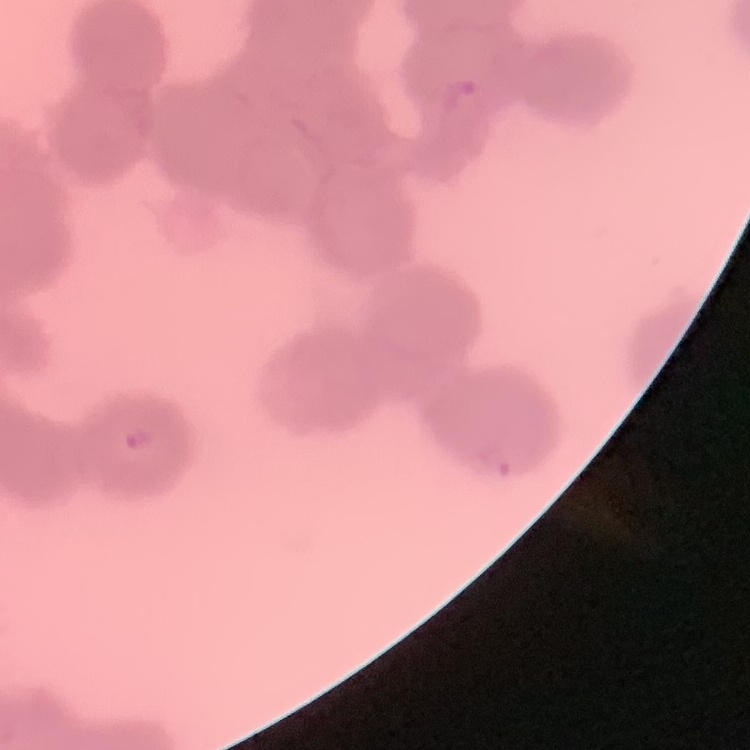
Summary:
  - Red blood cell morphology: rouleaux formation
  - Image type: square crop of a larger photomicrograph
  - Stain: Field's or Giemsa
  - Preparation: thin peripheral smear